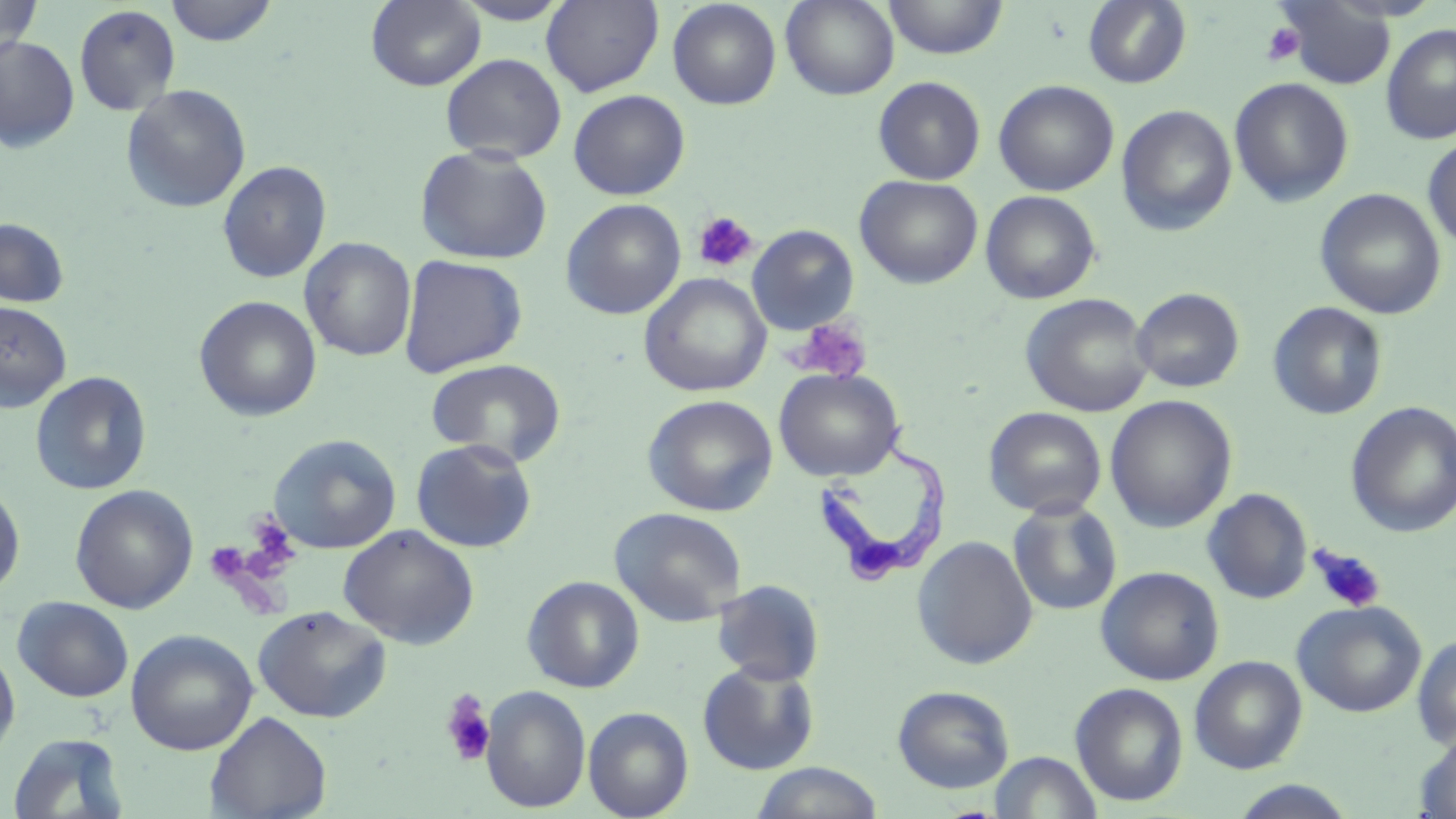
Approximate bounding boxes as (x1, y1, x2, y2) in pixels. Platelet locations: (1261, 22, 1305, 66), (693, 211, 759, 273), (789, 317, 873, 384), (243, 513, 300, 578), (204, 542, 251, 585), (1310, 545, 1386, 614), (440, 689, 498, 767). Trypanosoma brucei locations: (810, 419, 951, 586). Uninfected red blood cell locations: (0, 0, 42, 61), (164, 0, 278, 47), (452, 0, 573, 25), (541, 0, 664, 96), (780, 0, 900, 100), (883, 0, 1008, 60), (1083, 0, 1192, 89), (366, 1, 486, 91), (667, 1, 782, 109), (1276, 1, 1398, 90), (74, 4, 181, 115), (1381, 23, 1456, 145), (0, 35, 79, 153), (440, 53, 567, 164), (873, 77, 985, 185), (1229, 77, 1354, 208), (993, 80, 1120, 196), (121, 84, 251, 214), (568, 89, 690, 200), (1117, 105, 1237, 236), (1422, 135, 1456, 251), (415, 145, 554, 265), (217, 160, 332, 283), (855, 175, 983, 289), (1314, 188, 1446, 319), (980, 191, 1100, 304), (561, 198, 686, 320), (0, 218, 69, 308), (746, 224, 859, 335), (299, 237, 416, 362), (398, 254, 528, 378), (639, 272, 771, 397), (1131, 287, 1245, 394), (1020, 293, 1155, 417), (193, 296, 322, 422), (0, 301, 72, 412), (1267, 302, 1387, 420), (425, 357, 567, 466), (774, 367, 905, 482), (30, 371, 152, 495), (642, 394, 778, 517), (1105, 394, 1237, 532), (1346, 402, 1456, 538), (983, 406, 1107, 519), (268, 433, 401, 554), (411, 438, 538, 554), (0, 482, 25, 597), (70, 484, 198, 614), (1202, 487, 1313, 604), (1007, 499, 1123, 616), (609, 506, 747, 627), (338, 524, 479, 649), (912, 535, 1038, 669), (1095, 566, 1225, 686), (522, 575, 645, 693), (712, 579, 825, 686), (12, 596, 134, 703), (1292, 600, 1427, 717), (253, 605, 392, 723), (126, 628, 258, 755), (1412, 632, 1456, 749), (0, 642, 21, 763), (1189, 655, 1307, 774), (697, 661, 820, 776), (1070, 682, 1189, 806), (480, 685, 591, 813), (892, 685, 1015, 794), (583, 706, 694, 819), (204, 711, 332, 818), (1415, 728, 1456, 818), (7, 732, 129, 818), (990, 751, 1102, 819), (750, 762, 885, 819), (1228, 780, 1360, 819). Slide-level diagnosis: Trypanosoma brucei. Optical microscopy. Single field of view. May-Grünwald-Giemsa stain. Image is 1456×819 pixels. 1000x magnification. Thin blood film.